Report the malaria status of this cell.
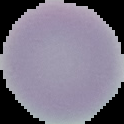

It is uninfected.

Summary:
  - Image type: segmented cell region on a black background
  - Image size: 124×124 pixels
  - Preparation: thin blood film